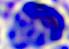 Micrograph. A white blood cell is shown. 400x magnification.